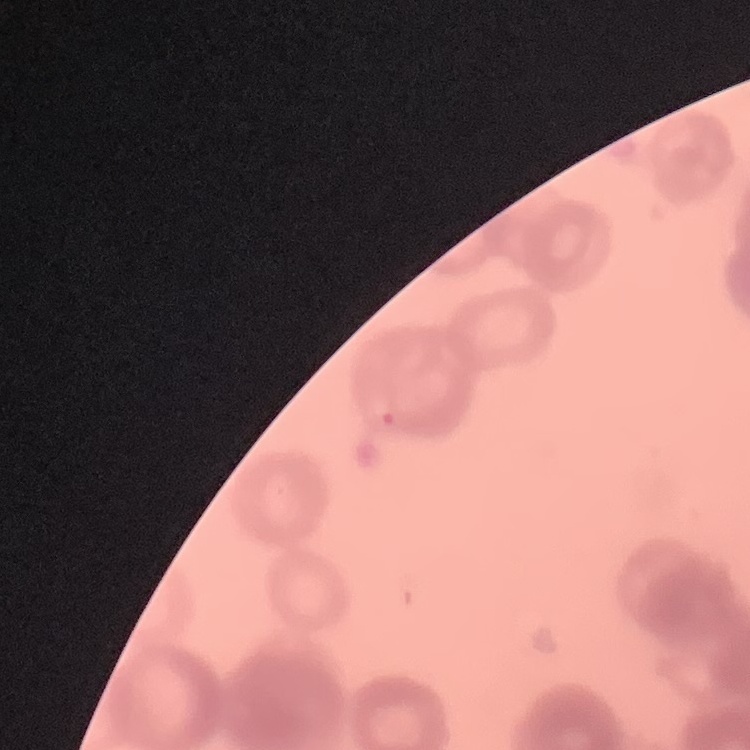
red blood cell morphology = rouleaux formation
stain = Field's or Giemsa
preparation = thin peripheral smear
image type = square crop of a larger photomicrograph